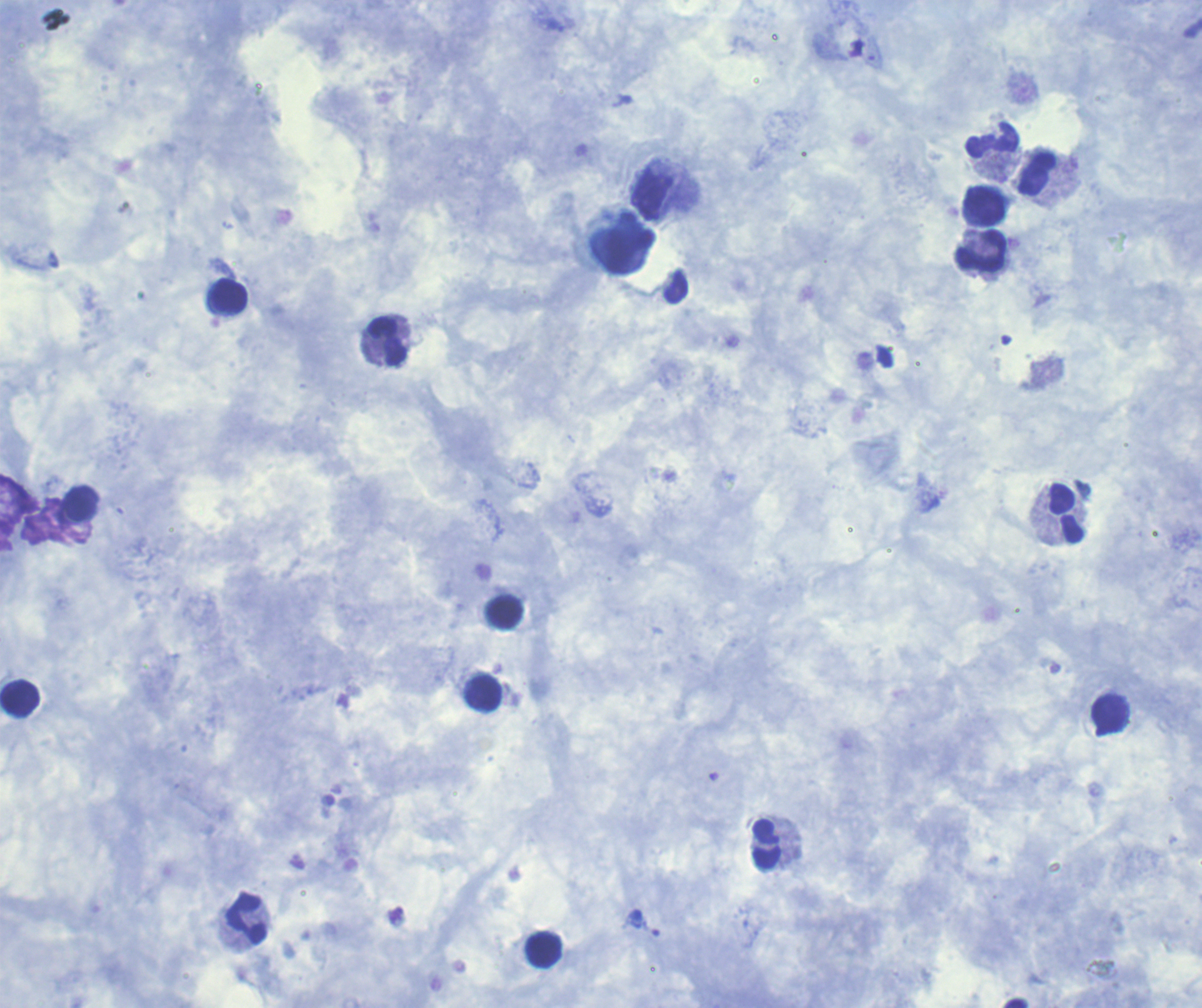

Approximate centers as (x, y) in pixels. Leukocyte locations: (992, 140), (1038, 174), (651, 193), (984, 206), (622, 243), (980, 250), (229, 295), (387, 342), (82, 502), (1067, 512), (505, 612), (484, 693), (20, 699), (1108, 713), (766, 845), (246, 917), (543, 951). Single field of view. Thick blood smear. Image is 1202×1008 pixels. 100x magnification. Previously used in an actual diagnosis. Background quality: good. Romanowsky stain. Result: no malaria parasites detected. Coloration quality: good.